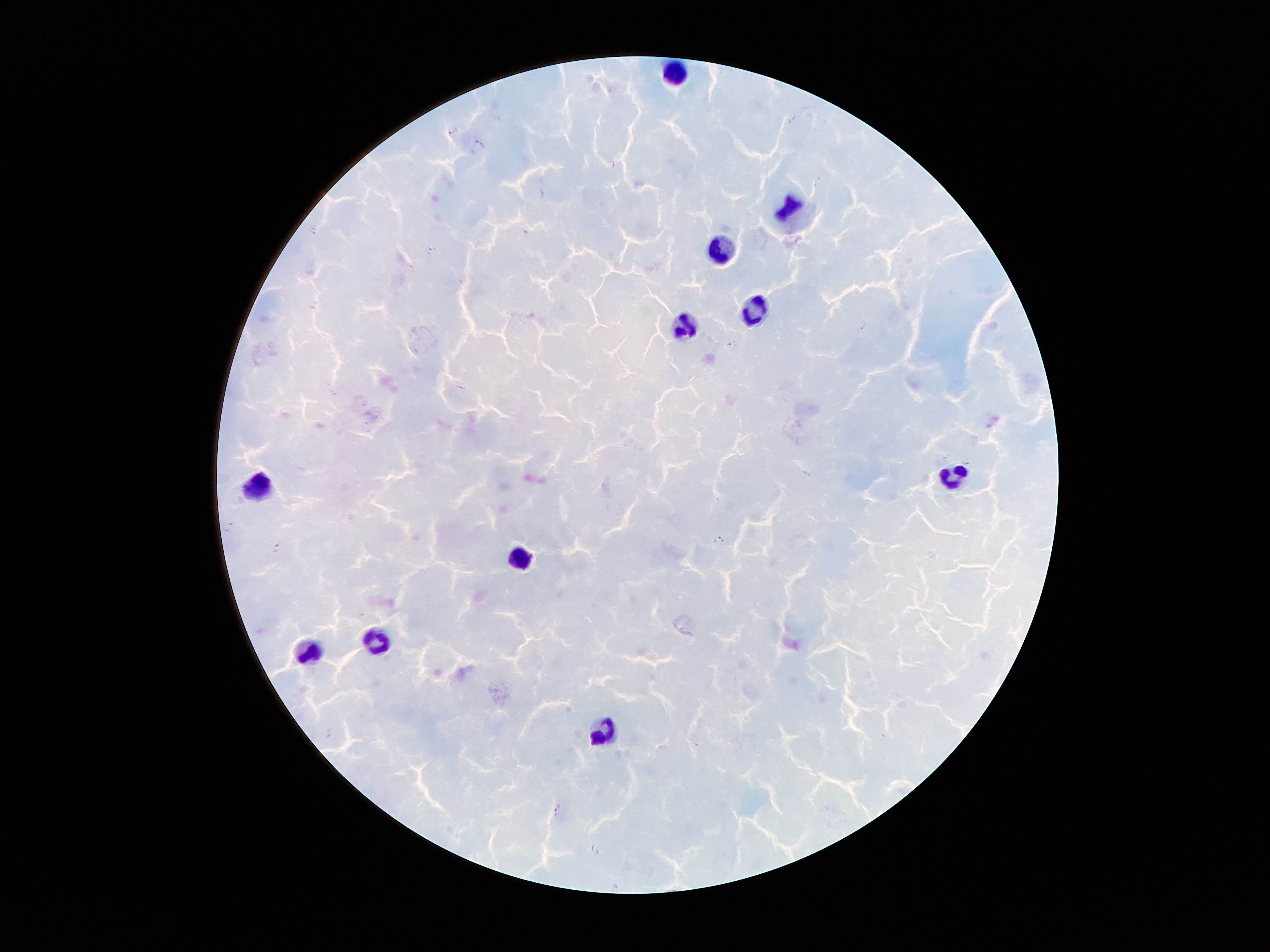 Approximate centers as [x, y] in pixels. Plasmodium parasite locations: [793, 119], [455, 130], [480, 141], [313, 230], [430, 250], [864, 326], [735, 345], [460, 386], [229, 525], [718, 539], [276, 547], [560, 809], [595, 849]. Leukocyte locations: [674, 73], [794, 211], [723, 252], [757, 309], [684, 326], [953, 478], [257, 484], [523, 554], [375, 641], [312, 650], [604, 733]. Smartphone photograph taken through the microscope eyepiece. Giemsa stain. Single field of view. Thick peripheral-blood smear. Patient malaria status: infected with Plasmodium falciparum. Image is 1270×952 pixels. 100x magnification.